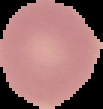
Summary:
  - Image type: cell region segmented out of the field of view; surrounding area masked to black
  - Image size: 103×109 pixels
  - Result: no Plasmodium parasites detected
  - Preparation: thin blood smear